Identify the parasite.
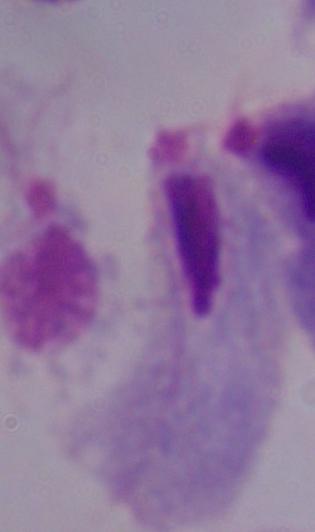

This is a trichomonad.

modality = micrograph
magnification = 1000x